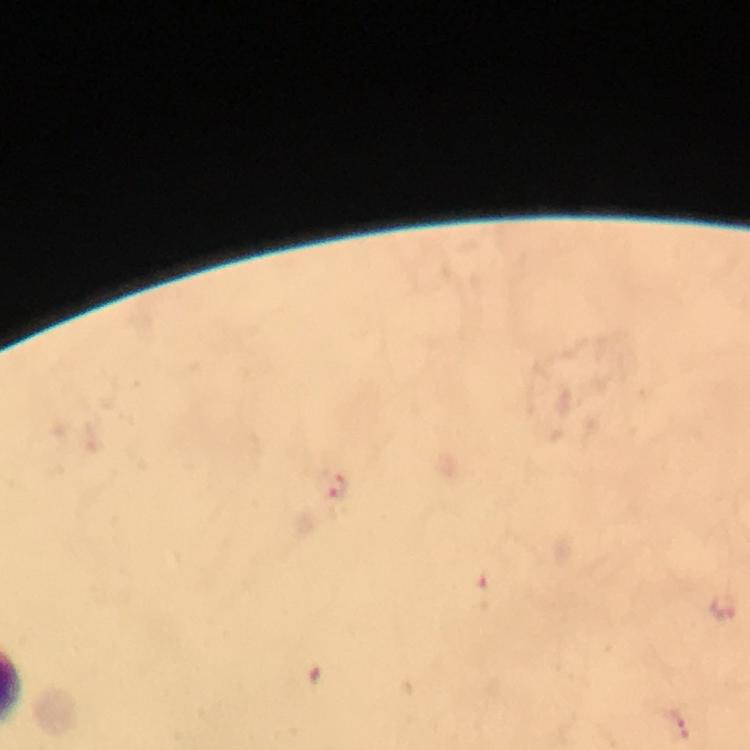
Approximate centers as [x, y] in pixels. Plasmodium parasite locations: [337, 487]. Image is 750×750 pixels. Photographed through the microscope with a smartphone camera. Immersion oil was used. Giemsa stain. At 100x magnification. Thick smear. Cropped region of a single field of view. From a diagnostic examination for malaria.